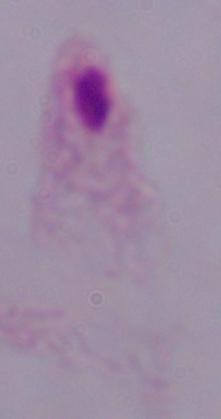

Summary:
  - Magnification: 1000x
  - Identification: trichomonad
  - Modality: micrograph